Point out each Plasmodium parasite and each leukocyte.
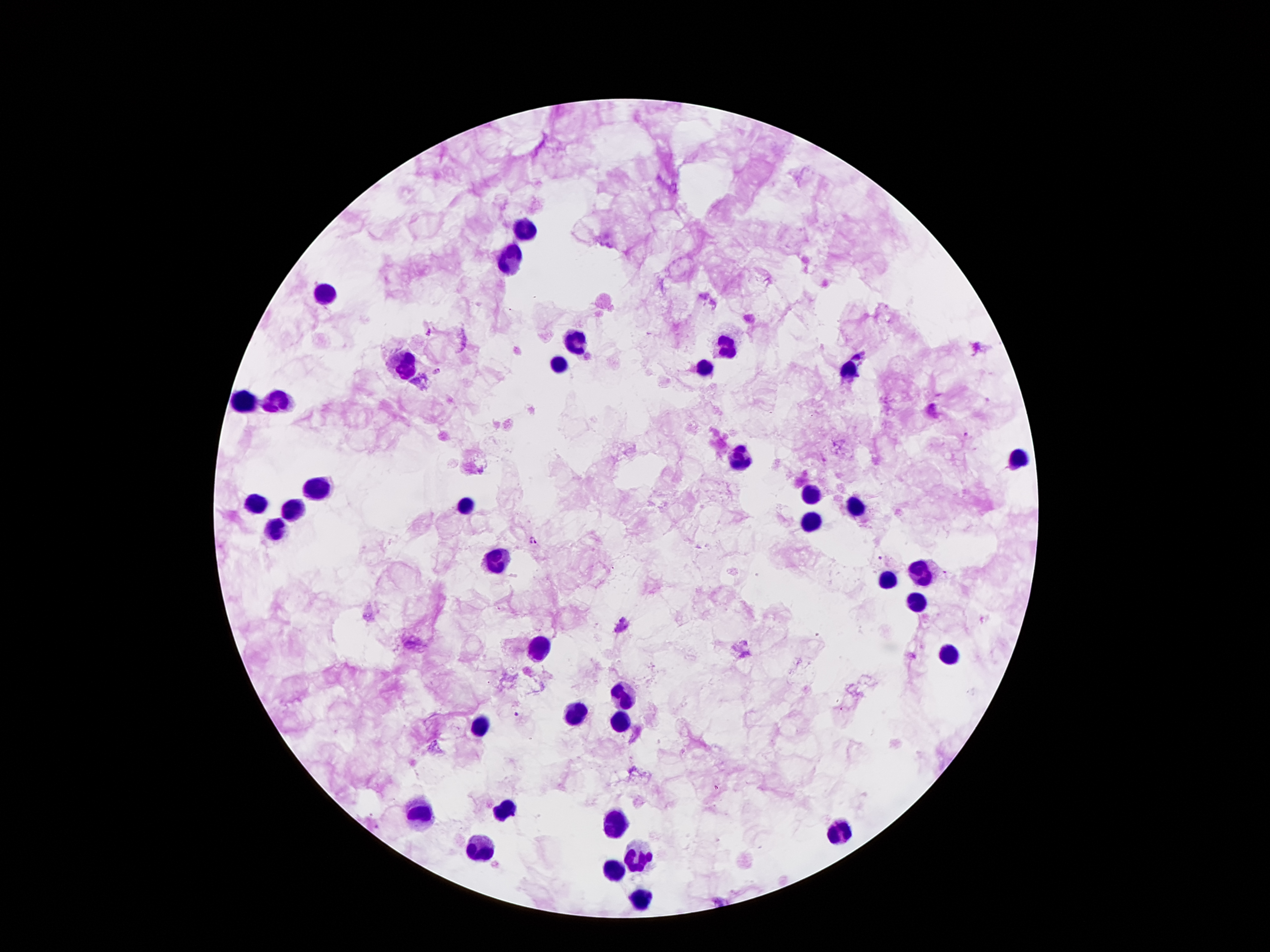
Approximate centers as (x, y) in pixels.
Plasmodium parasites: (429, 331), (437, 370), (966, 436), (533, 540), (879, 559), (622, 626), (518, 715).
Leukocytes: (523, 229), (512, 262), (325, 292), (575, 339), (726, 348), (560, 365), (406, 367), (705, 367), (845, 371), (245, 401), (278, 401), (1017, 457), (740, 458), (320, 485), (810, 493), (255, 504), (463, 505), (856, 505), (292, 509), (812, 521), (276, 532), (497, 561), (919, 572), (885, 579), (919, 600), (540, 647), (950, 651), (621, 695), (579, 712), (621, 724), (483, 728), (504, 810), (420, 813), (612, 821), (840, 836), (479, 852), (635, 853), (612, 866), (642, 901).

Summary:
  - Capture: smartphone through the microscope eyepiece
  - Preparation: thick blood film
  - Patient malaria status: positive for Plasmodium falciparum
  - Image size: 1270×952 pixels
  - Magnification: 100x
  - Field of view: single
  - Stain: Giemsa